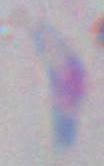
Toxoplasma gondii is shown. Photomicrograph. 1000x magnification.